Give the extent of all uninfected red blood cells.
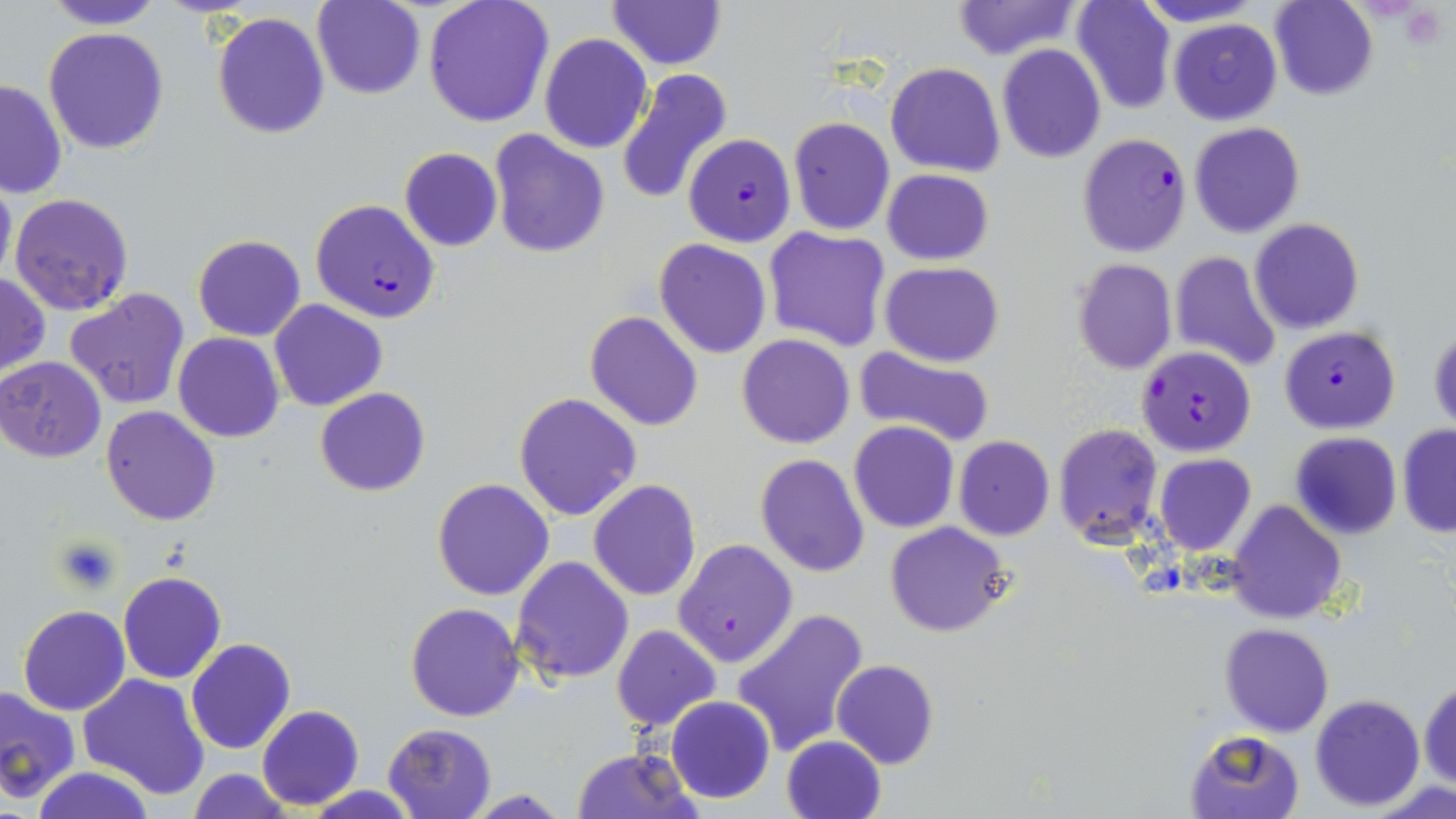

Approximate bounding boxes as (x1, y1, x2, y2) in pixels.
Uninfected red blood cells: (44, 0, 164, 29), (314, 0, 425, 100), (423, 0, 555, 127), (1072, 0, 1177, 115), (1134, 0, 1264, 27), (1269, 0, 1378, 100), (606, 1, 726, 70), (950, 1, 1083, 59), (211, 12, 331, 139), (1169, 18, 1281, 125), (43, 27, 167, 155), (540, 33, 651, 153), (997, 44, 1107, 164), (885, 63, 1005, 178), (615, 69, 732, 206), (0, 79, 68, 198), (788, 116, 895, 235), (1188, 121, 1305, 237), (489, 130, 610, 260), (399, 147, 502, 252), (881, 169, 993, 265), (0, 173, 15, 285), (9, 192, 134, 318), (1250, 218, 1364, 334), (763, 228, 891, 351), (192, 234, 307, 342), (653, 240, 773, 358), (1169, 252, 1282, 372), (1072, 258, 1178, 374), (880, 262, 1005, 365), (0, 271, 49, 379), (64, 287, 191, 411), (268, 299, 388, 412), (585, 310, 703, 430), (1428, 328, 1456, 433), (173, 333, 283, 442), (736, 334, 856, 449), (854, 346, 996, 450), (1, 357, 106, 462), (315, 387, 430, 496), (513, 392, 642, 521), (99, 406, 222, 526), (849, 422, 958, 533), (1053, 424, 1162, 545), (1397, 425, 1456, 538), (1289, 432, 1402, 539), (953, 436, 1055, 539), (1153, 453, 1257, 556), (755, 454, 869, 576), (432, 479, 556, 601), (589, 480, 702, 602), (1226, 499, 1347, 624), (886, 522, 1013, 637), (674, 539, 797, 667), (512, 555, 634, 686), (118, 571, 227, 685), (406, 601, 525, 722), (17, 605, 130, 715), (731, 606, 870, 759), (1220, 623, 1333, 737), (611, 624, 720, 730), (186, 639, 295, 755), (831, 659, 940, 769), (77, 673, 210, 799), (1420, 678, 1455, 790), (0, 687, 80, 803), (1310, 693, 1424, 811), (664, 696, 775, 803), (257, 704, 364, 811), (382, 722, 497, 819), (1184, 727, 1309, 819), (782, 735, 887, 819), (572, 748, 697, 818), (28, 766, 156, 819), (187, 769, 293, 818), (1370, 777, 1456, 819), (463, 791, 571, 819).

{
  "slide_level_diagnosis": "Plasmodium falciparum",
  "image_size": "1456×819 pixels",
  "magnification": "1000x",
  "preparation": "thin blood film",
  "field_of_view": "one of a larger specimen",
  "stain": "May-Grünwald-Giemsa",
  "plasmodium_falciparum_infected_red_blood_cell_locations": "approximate bounding boxes as (x1, y1, x2, y2) in pixels: (684, 133, 796, 247), (1076, 134, 1191, 258), (309, 199, 439, 322), (1279, 325, 1400, 432), (1136, 345, 1257, 456)",
  "modality": "optical microscopy",
  "platelet_locations": "approximate bounding boxes as (x1, y1, x2, y2) in pixels: (52, 535, 122, 595)"
}